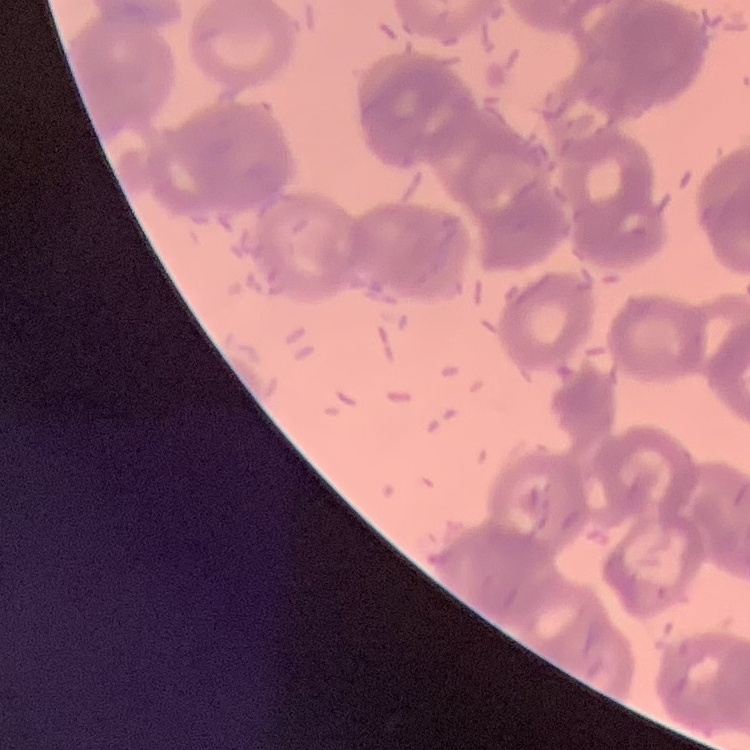
The red blood cells exhibit rouleaux formation. Thin blood film. Stained with either Field's or Giemsa. Square crop of a larger photomicrograph.